Classify this cell by malaria status.
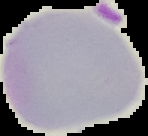

Uninfected.

Summary:
  - Image type: segmented cell region on a black background
  - Preparation: thin blood film
  - Image size: 148×136 pixels